Describe the morphology of the erythrocytes.
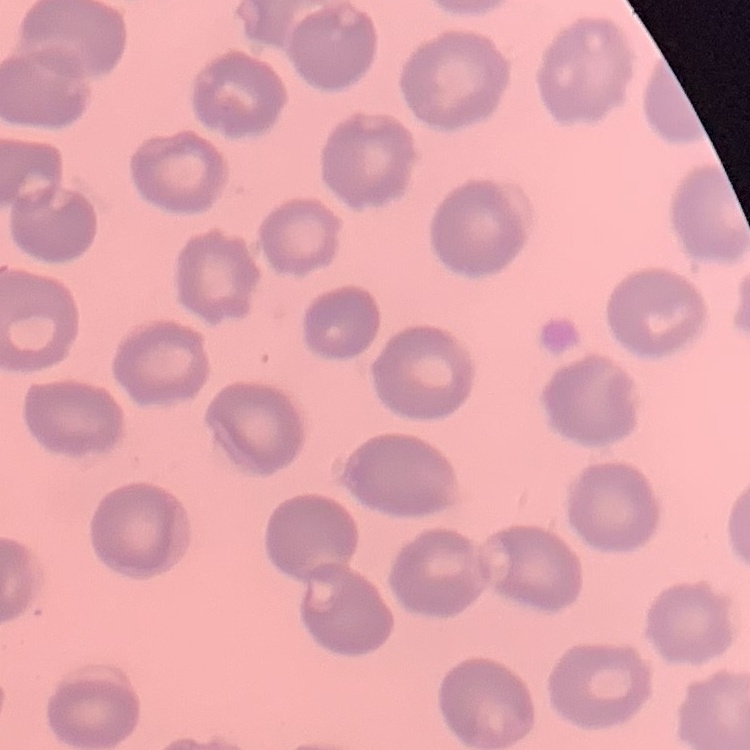
They show no rouleaux formation.

Summary:
  - Image type: square crop of a larger photomicrograph
  - Stain: Field's or Giemsa
  - Preparation: thin peripheral smear